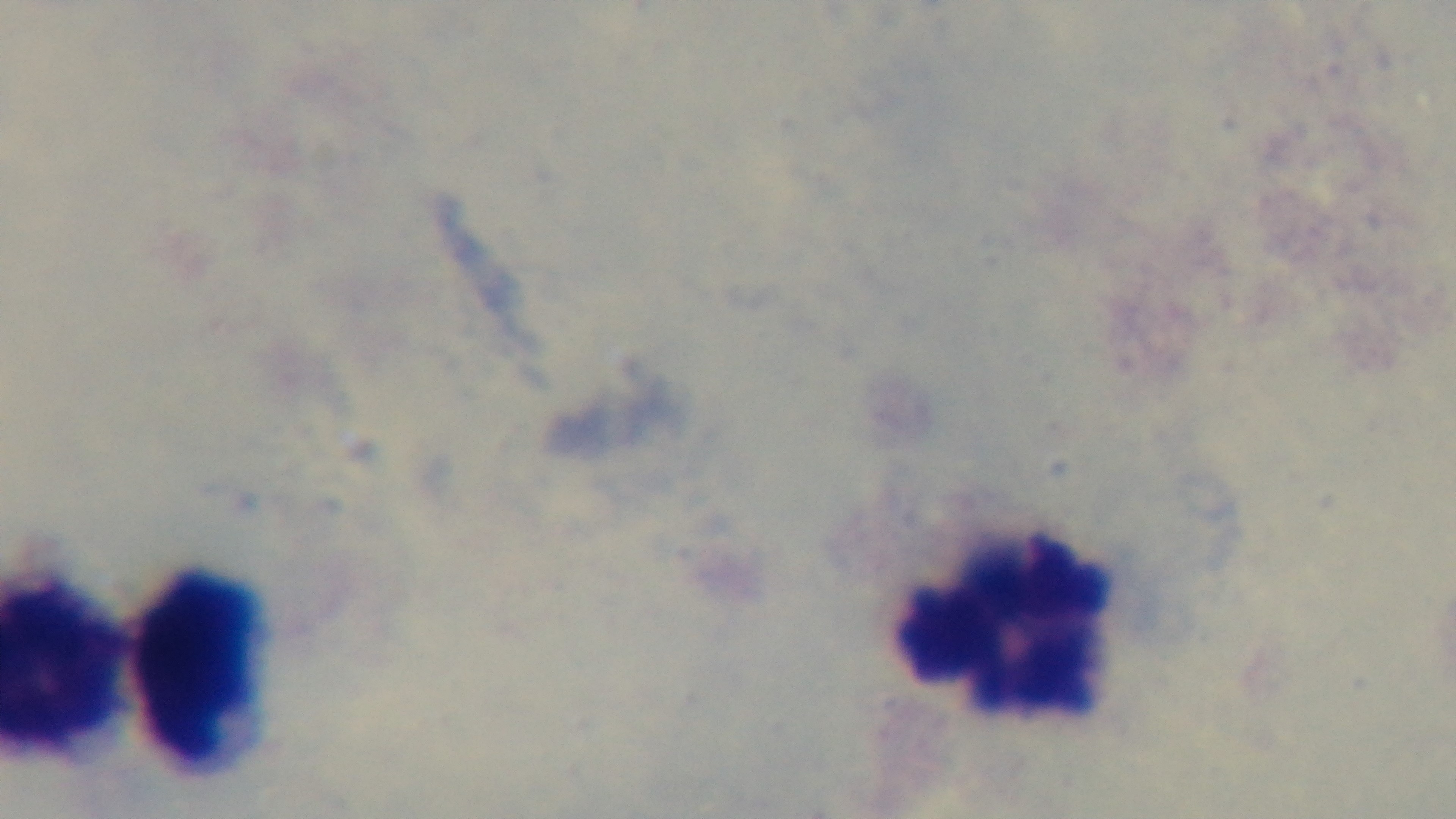 Giemsa-stained. One field from the slide. Mounted 4K digital camera. Preparation: thick smear. 100x oil-immersion objective. Malaria status: negative. Light microscopy.